Classify this cell by malaria status.
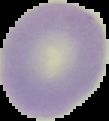
It is uninfected.

image_type: cell region segmented out of the field of view; surrounding area masked to black
preparation: thin blood smear
image_size: 109×121 pixels